State which parasite is depicted.
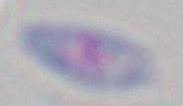
This is Toxoplasma gondii.

magnification = 1000x
modality = micrograph